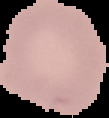

Result: negative for malaria parasites. Cell region segmented out of the field of view; the surrounding area is masked to black. Image is 109×118 pixels. From a thin blood smear.